Give the position of every Plasmodium parasite.
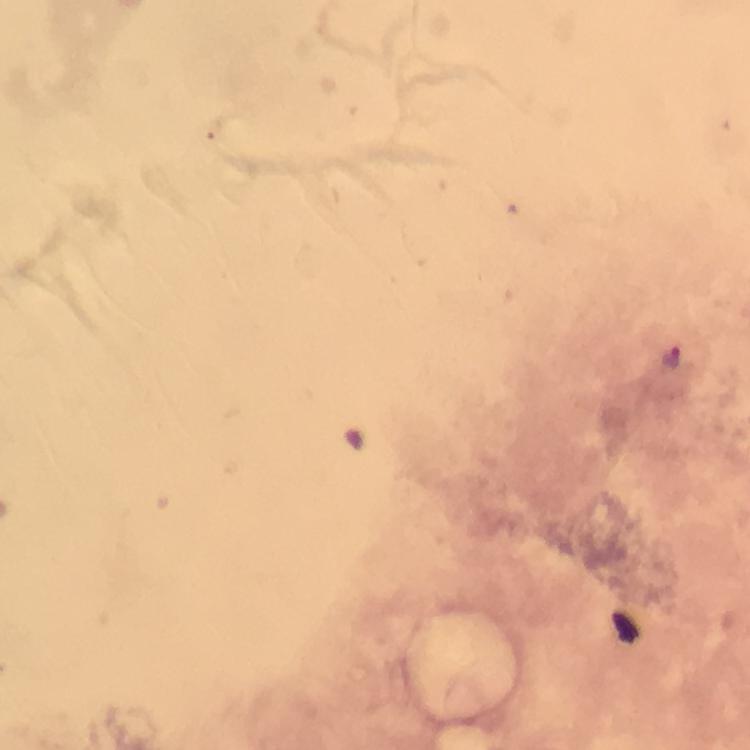

Approximate centers as {x, y} in pixels.
Plasmodium parasites: {673, 358}.

preparation = thick blood film
image size = 750×750 pixels
immersion oil = used
capture = smartphone camera through the microscope
stain = Giemsa
context = from a malaria diagnostic workup
magnification = 100x
cropped from = one field of view